Assess this cell for malaria.
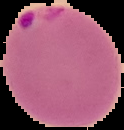
Parasitized.

image type = segmented cell region with the area outside set to black
preparation = thin blood smear
image size = 124×130 pixels